State the blood parasite species.
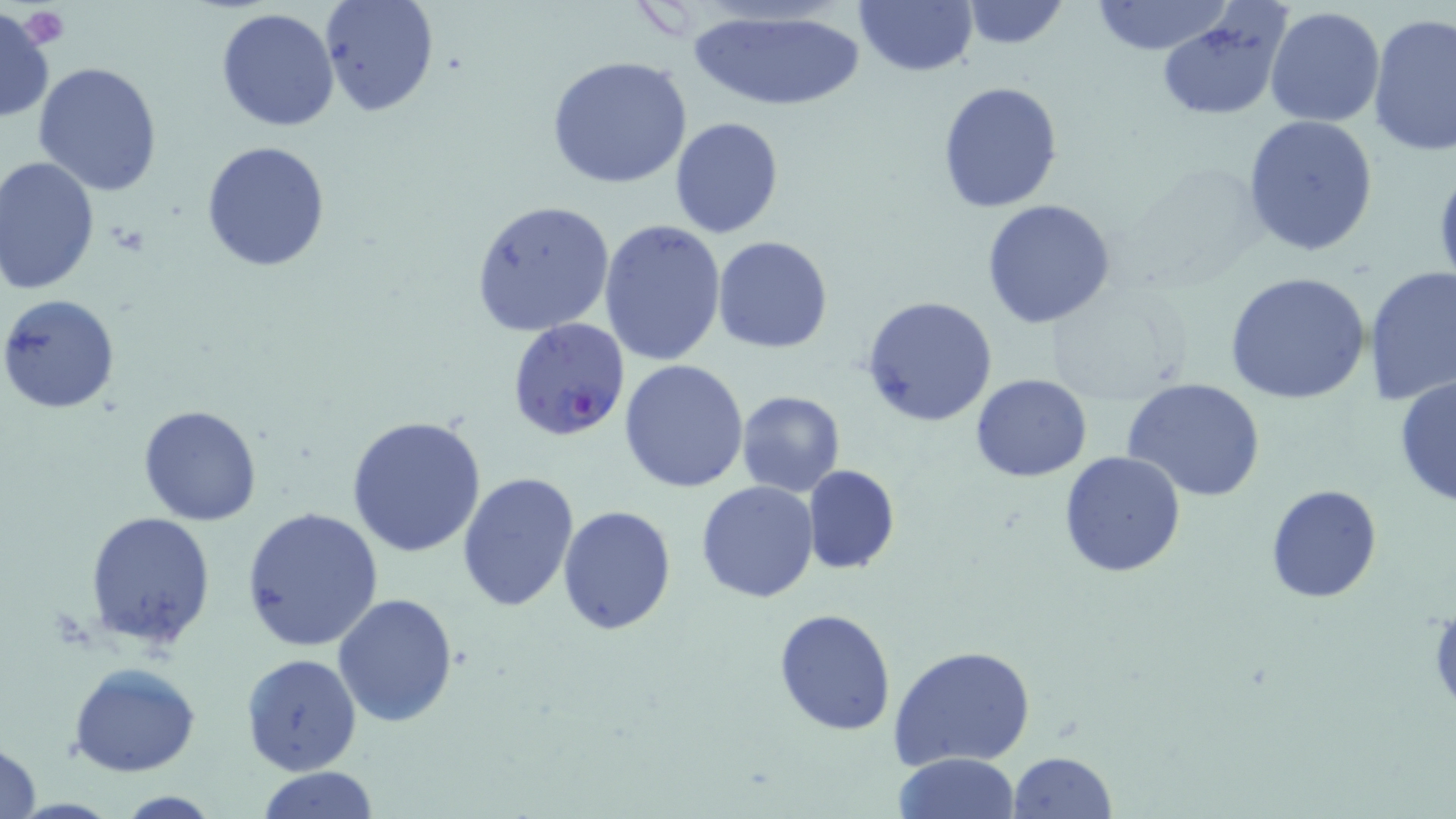

Plasmodium falciparum.

magnification: 1000x
field_of_view: single
image_size: 1456×819 pixels
uninfected_red_blood_cell_locations: 'approximate bounding boxes as (x1, y1, x2, y2) in pixels: (318, 0, 440, 117), (853, 0, 980, 78), (958, 1, 1069, 51), (1090, 1, 1232, 55), (0, 5, 55, 124), (680, 5, 872, 113), (215, 6, 341, 133), (1264, 7, 1388, 128), (1155, 12, 1285, 120), (1368, 14, 1456, 161), (545, 54, 697, 191), (33, 60, 163, 195), (937, 80, 1065, 215), (1241, 115, 1381, 258), (670, 116, 783, 239), (201, 140, 332, 271), (0, 156, 100, 295), (980, 198, 1117, 329), (469, 200, 614, 335), (599, 218, 727, 366), (712, 236, 834, 354), (1362, 264, 1456, 407), (1224, 271, 1372, 407), (1045, 288, 1187, 407), (0, 293, 121, 416), (862, 295, 1000, 429), (619, 357, 750, 492), (970, 374, 1092, 482), (1393, 375, 1456, 508), (1121, 378, 1267, 503), (735, 389, 845, 496), (138, 404, 263, 527), (1089, 407, 1259, 551), (346, 414, 487, 559), (1057, 450, 1186, 578), (802, 465, 900, 574), (457, 471, 582, 614), (696, 481, 820, 603), (1265, 484, 1382, 604), (557, 503, 676, 636), (242, 507, 385, 652), (85, 511, 218, 650), (333, 592, 458, 726), (773, 606, 894, 736), (889, 645, 1036, 771), (240, 653, 363, 775), (66, 662, 202, 777), (1, 737, 42, 819), (1009, 751, 1116, 819), (893, 752, 1022, 818), (252, 767, 382, 819), (109, 790, 224, 818)'
modality: light microscopy
stain: May-Grünwald-Giemsa
preparation: thin blood smear
platelet_locations: 'approximate bounding boxes as (x1, y1, x2, y2) in pixels: (18, 6, 69, 49), (1428, 602, 1456, 716)'
plasmodium_falciparum_infected_red_blood_cell_locations: 'approximate bounding boxes as (x1, y1, x2, y2) in pixels: (506, 317, 631, 440)'